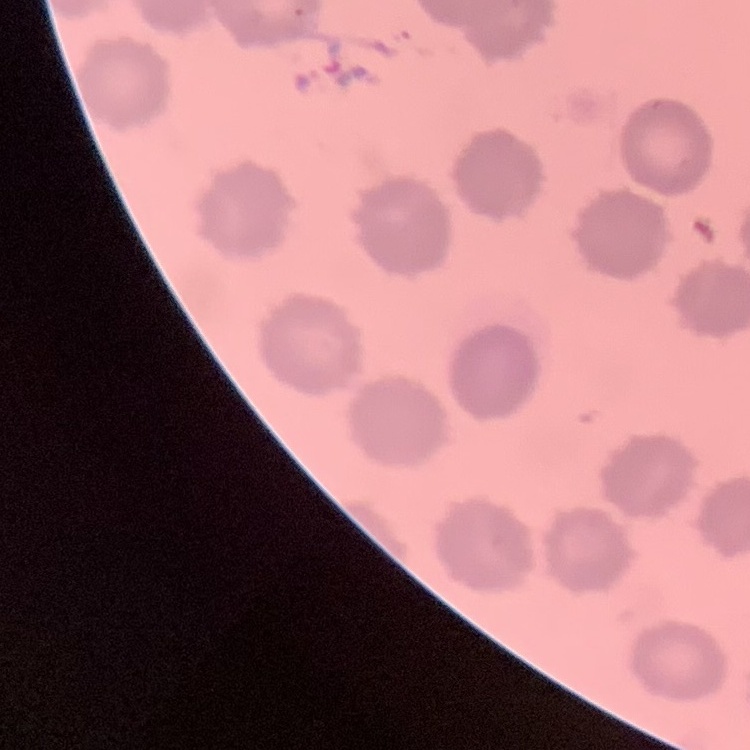

The erythrocytes show no rouleaux formation. Square crop of a larger photomicrograph. Stained with either Field's or Giemsa. Thin blood film.